Describe the morphology of the erythrocytes.
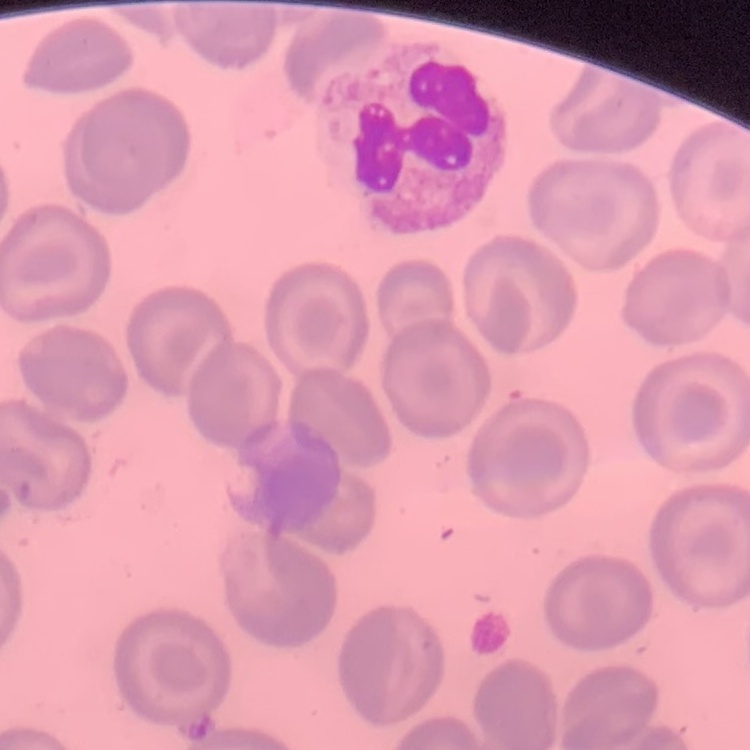
No rouleaux formation.

Summary:
  - Image type: one tile cut from a larger photomicrograph
  - Preparation: thin peripheral smear
  - Stain: Field's or Giemsa